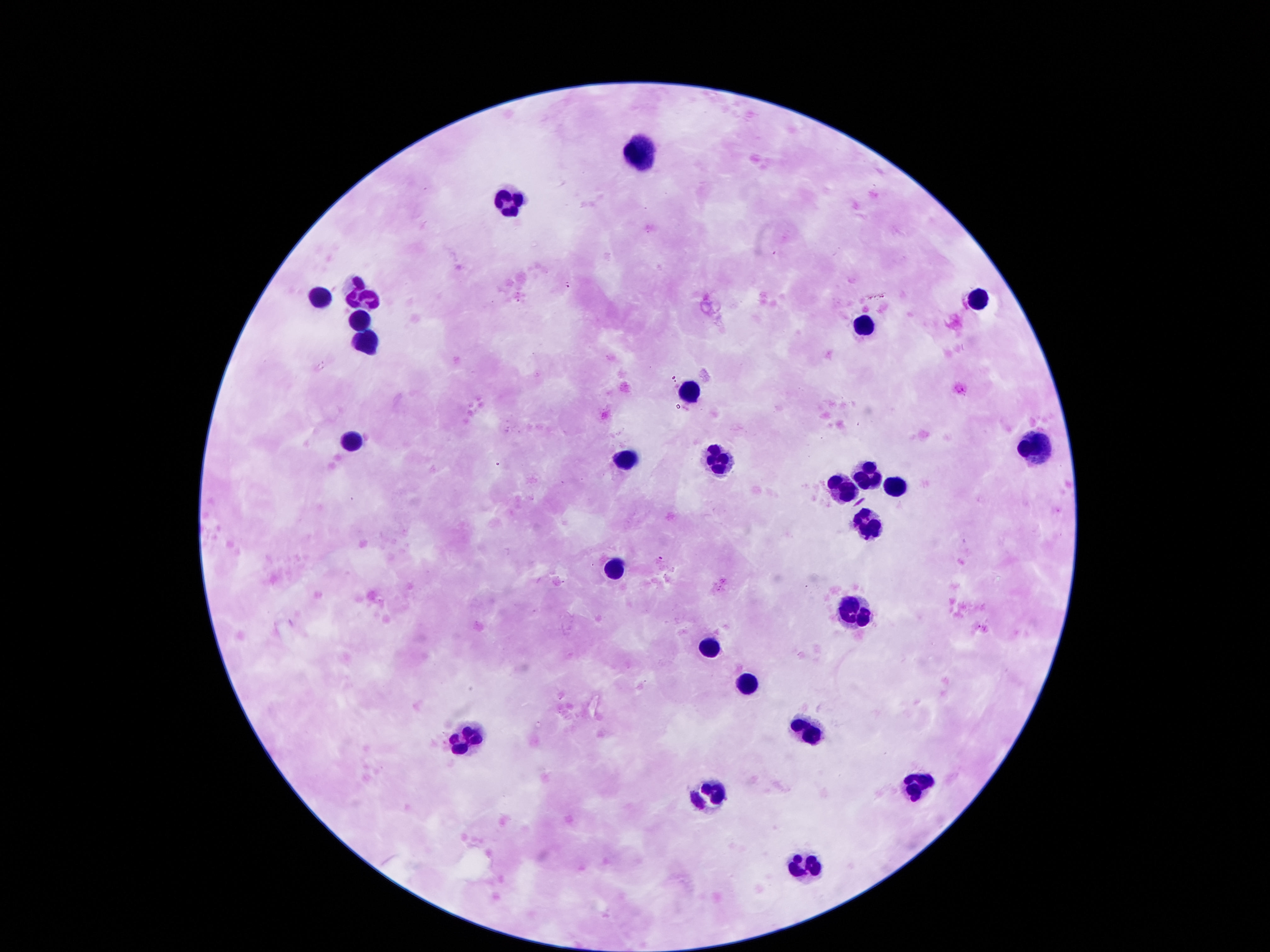

Approximate centers as [x, y] in pixels.
Summary:
  - Leukocyte locations: [638, 155], [506, 204], [362, 291], [977, 291], [317, 294], [359, 320], [863, 330], [365, 342], [695, 389], [347, 441], [1034, 450], [623, 459], [713, 459], [869, 470], [896, 485], [842, 488], [869, 527], [617, 564], [851, 618], [710, 648], [746, 684], [809, 732], [470, 737], [917, 785], [707, 797], [806, 869]
  - Field of view: one from this slide
  - Image size: 1270×952 pixels
  - Capture: smartphone camera through the microscope eyepiece
  - Magnification: 100x
  - Preparation: thick blood film
  - Stain: Giemsa
  - Patient malaria status: negative